Comment on the morphology of the red blood cells.
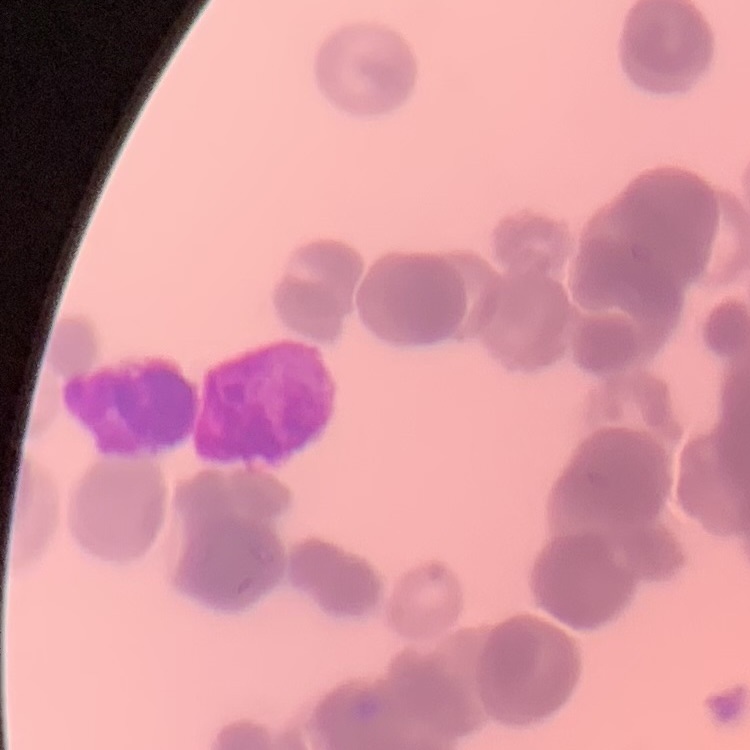
Rouleaux formation.

preparation: thin blood smear
stain: Field's or Giemsa
image_type: one tile cut from a larger photomicrograph